Name the parasite shown.
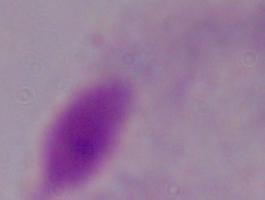

A trichomonad.

Summary:
  - Modality: photomicrograph
  - Magnification: 1000x